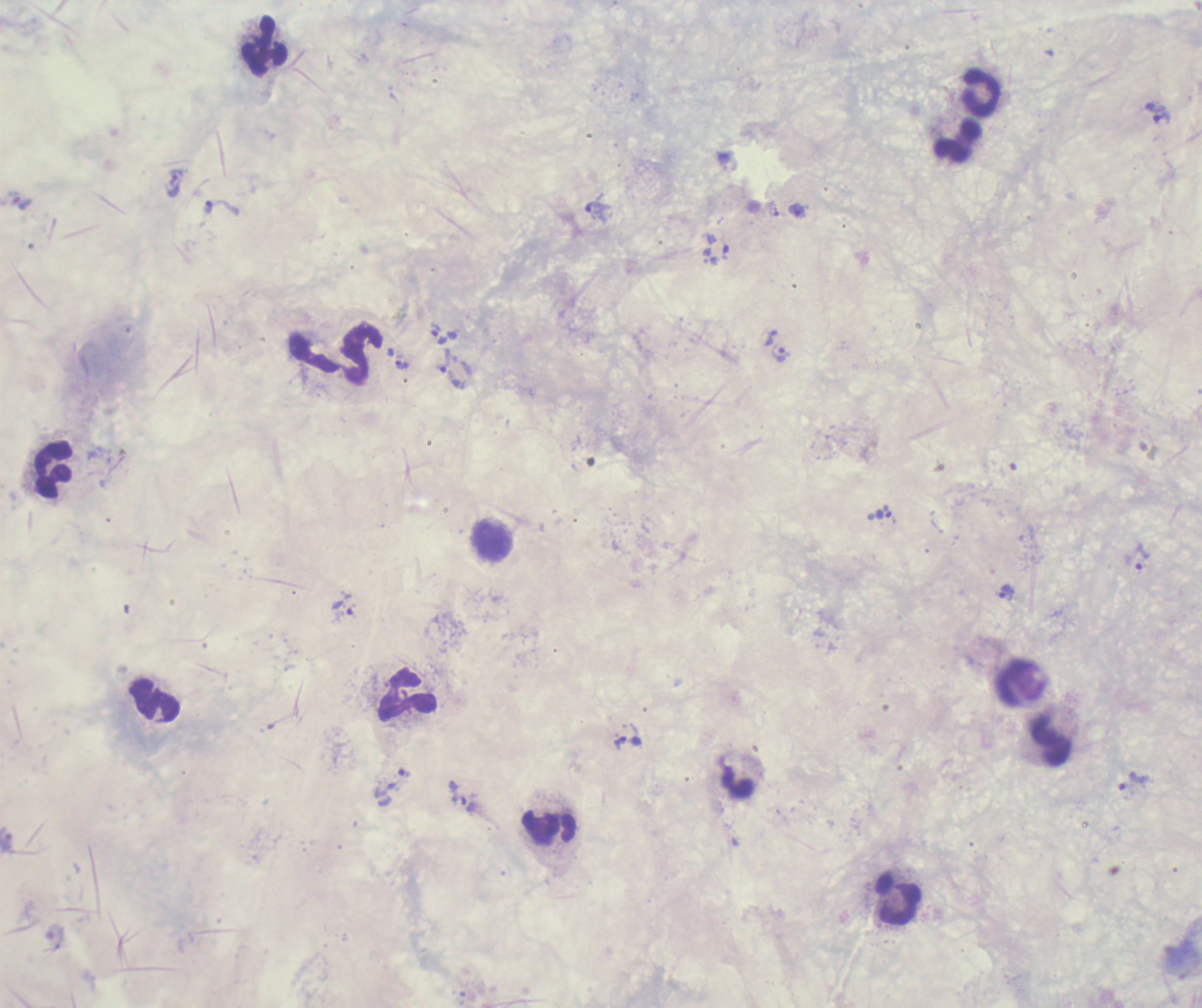

Approximate centers as [x, y] in pixels.
Summary:
  - Trophozoite locations: [1158, 113], [175, 181], [222, 208], [598, 212], [726, 250], [438, 333], [781, 353], [443, 361], [402, 364], [887, 511], [1142, 557], [1007, 592], [342, 610], [620, 743], [404, 772], [1133, 782], [463, 803]
  - Leukocyte locations: [265, 46], [982, 92], [958, 141], [54, 471], [492, 540], [407, 694], [1051, 741], [548, 825], [899, 899]
  - Background quality: poor
  - Stain: Romanowsky
  - Field of view: one from this slide
  - Preparation: thick blood film
  - Coloration quality: bad
  - Context: previously used in an actual diagnosis
  - Magnification: 100x
  - Result: malaria parasites identified
  - Image size: 1202×1008 pixels